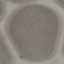

malaria status = uninfected
image type = cell patch, automatically extracted from a larger field of view and resized to 64 × 64 pixels
capture = smartphone camera at the microscope eyepiece
preparation = thin blood film
stain = Giemsa